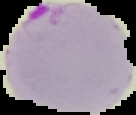

Segmented cell region on a black background. From a thin blood film. Image is 136×115 pixels. Result: Plasmodium parasites detected.